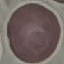
malaria status = uninfected
preparation = thin smear
stain = Giemsa
image type = cell patch, automatically extracted from a larger field of view and resized to 64 × 64 pixels
capture = smartphone through the microscope eyepiece